Outline each Babesia divergens-infected red blood cell.
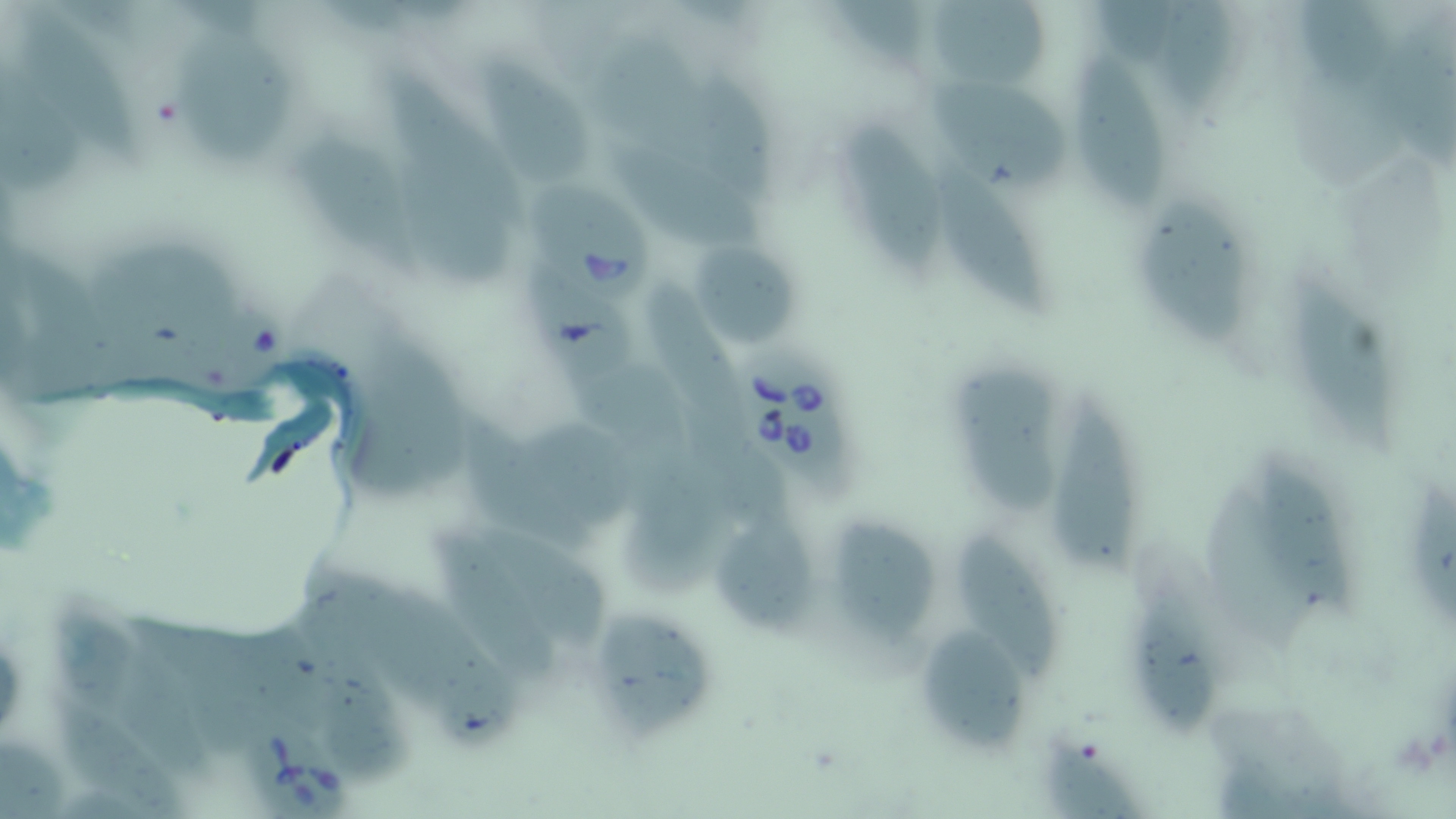

Approximate bounding boxes as [x1, y1, x2, y2] in pixels.
Babesia divergens-infected red blood cells: [531, 179, 658, 308], [737, 347, 852, 486], [227, 720, 361, 819].

Summary:
  - Uninfected red blood cell locations: [1297, 0, 1389, 93], [934, 2, 1052, 96], [1164, 2, 1234, 111], [22, 9, 139, 171], [174, 33, 296, 166], [1076, 55, 1166, 215], [474, 56, 595, 189], [692, 76, 778, 203], [921, 81, 1069, 193], [845, 123, 946, 280], [301, 133, 425, 280], [611, 146, 767, 256], [398, 149, 515, 293], [936, 161, 1057, 319], [1143, 200, 1249, 352], [694, 239, 803, 346], [523, 265, 643, 386], [1292, 274, 1399, 456], [648, 288, 744, 438], [569, 359, 695, 477], [956, 366, 1061, 520], [1047, 396, 1139, 578], [460, 416, 591, 548], [1256, 458, 1357, 618], [1403, 485, 1456, 630], [719, 513, 813, 640], [835, 520, 945, 645], [480, 529, 612, 652], [433, 531, 564, 691], [952, 536, 1060, 688], [1134, 599, 1218, 738], [598, 611, 716, 737], [916, 630, 1029, 750], [57, 702, 186, 817], [1041, 736, 1136, 818]
  - Slide-level diagnosis: Babesia divergens
  - Preparation: thin blood film
  - Field of view: one of a larger specimen
  - Image size: 1456×819 pixels
  - Stain: May-Grünwald-Giemsa
  - Magnification: 1000x
  - Modality: light microscopy